Identify the parasite.
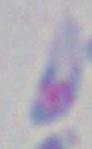

Toxoplasma gondii.

modality = photomicrograph
magnification = 1000x